Give the position of every malaria parasite.
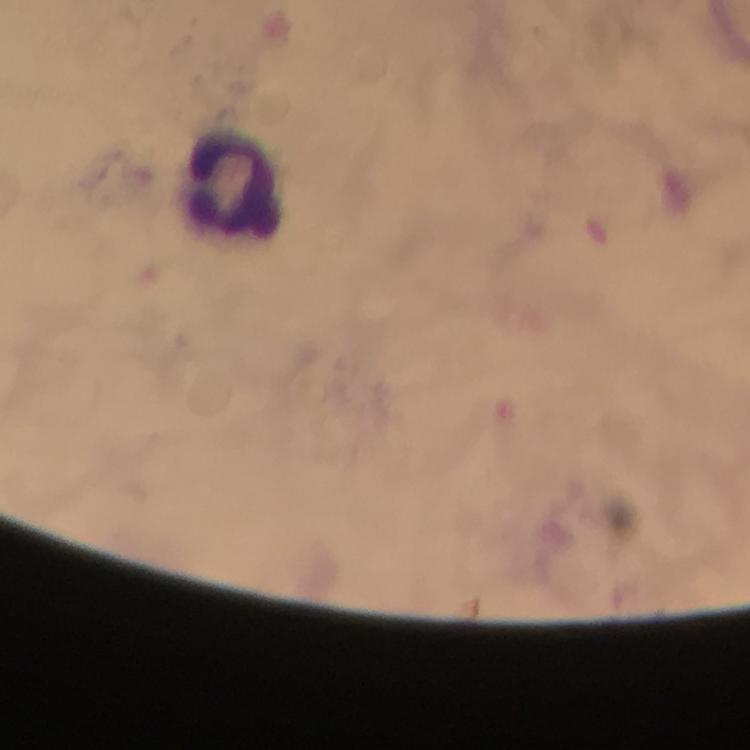

No malaria parasites seen.

{
  "cropped_from": "one field of view",
  "magnification": "100x",
  "stain": "Giemsa",
  "leukocyte_locations": "approximate centers as {x, y} in pixels: {232, 182}",
  "context": "from a malaria diagnostic workup",
  "image_size": "750×750 pixels",
  "capture": "smartphone mounted on the microscope",
  "preparation": "thick blood smear",
  "immersion_oil": "applied"
}